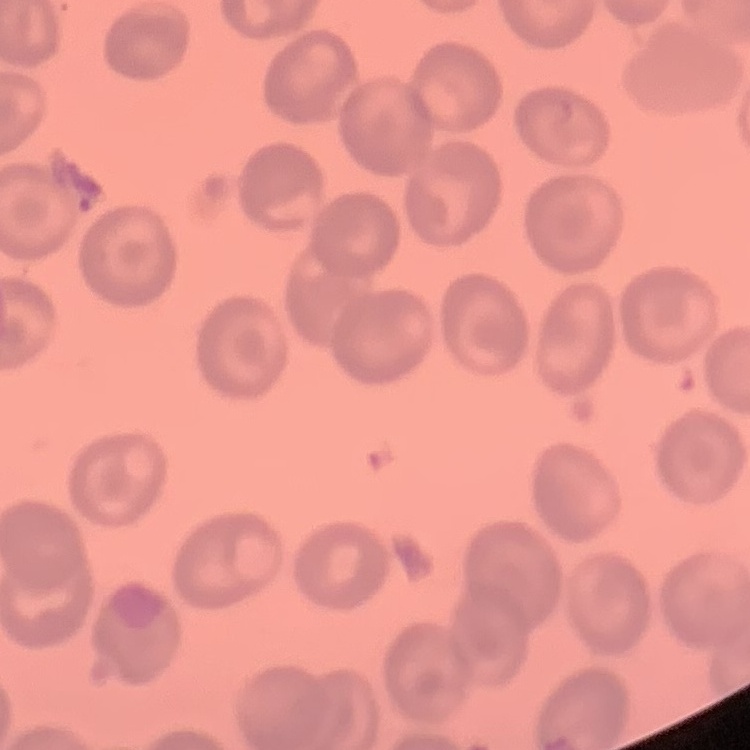
The erythrocytes exhibit no rouleaux formation. Thin blood film. One tile cut from a larger photomicrograph. Field's or Giemsa stain.